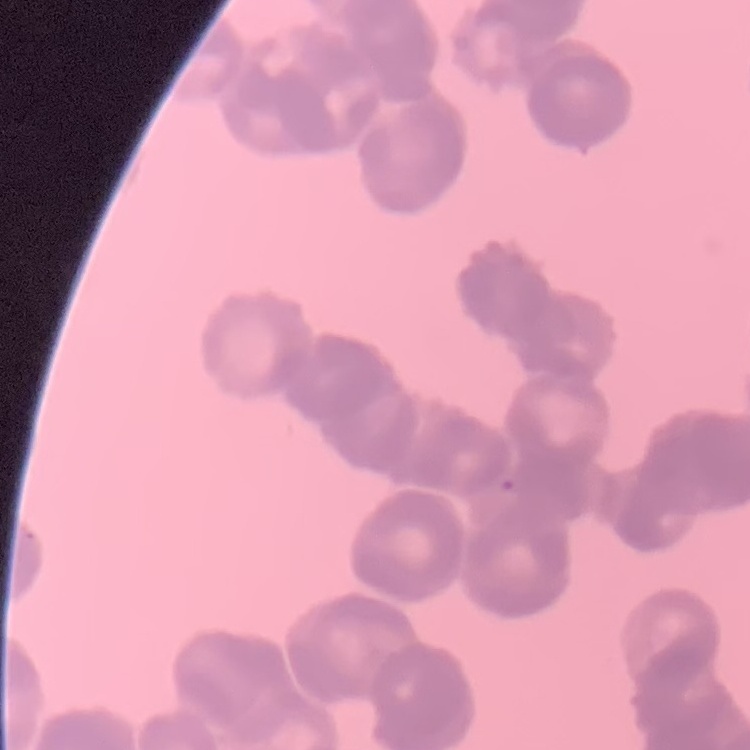

Summary:
  - Red blood cell morphology: rouleaux formation
  - Stain: Field's or Giemsa
  - Preparation: thin blood film
  - Image type: square crop of a larger photomicrograph